Point out each Plasmodium parasite.
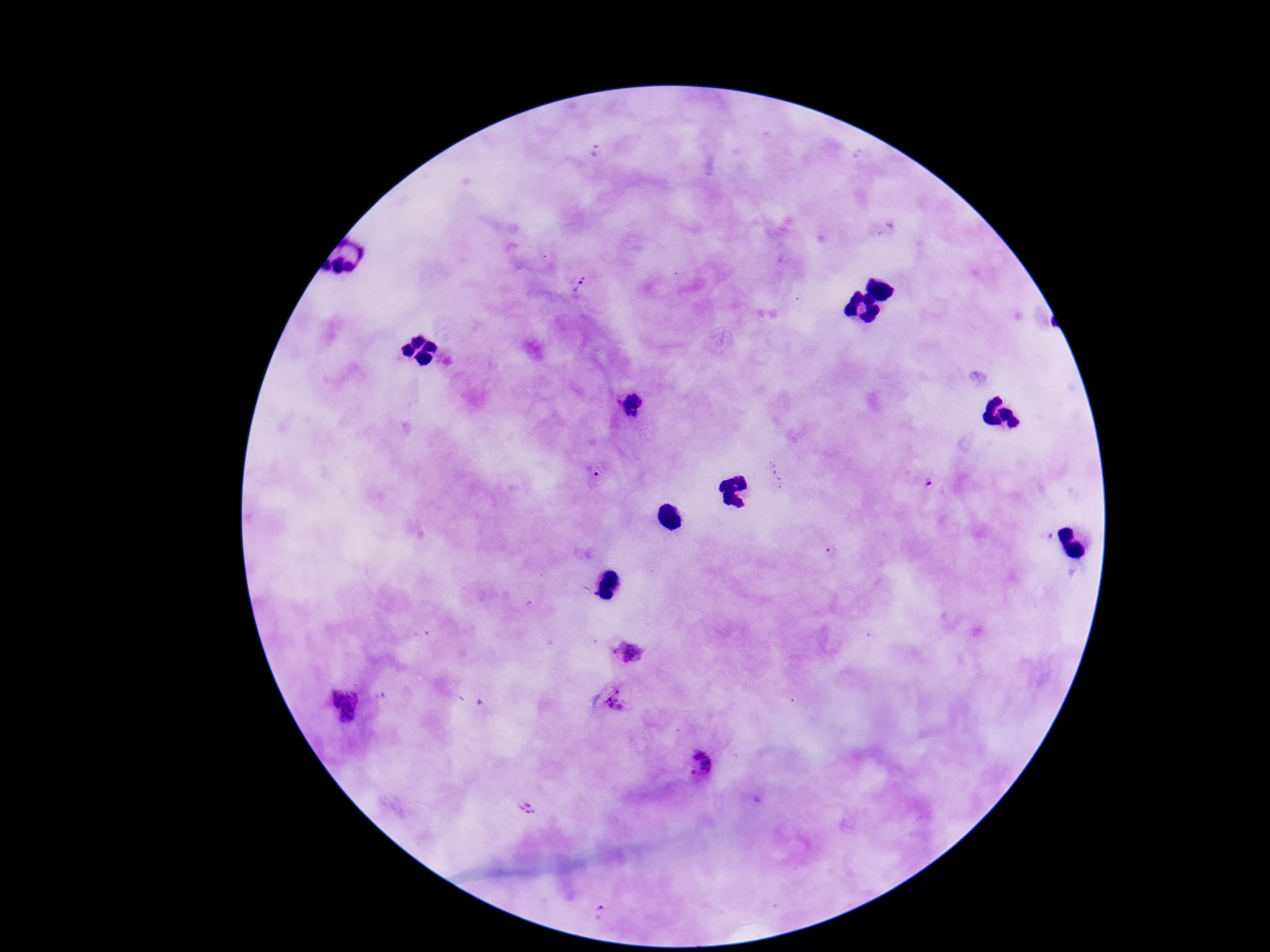
Approximate object centers, in pixels from the top-left corner.
Plasmodium parasites: (x=595, y=152), (x=580, y=283), (x=632, y=402), (x=596, y=474), (x=929, y=486), (x=1045, y=536), (x=831, y=550), (x=629, y=653), (x=379, y=696), (x=615, y=703), (x=344, y=705), (x=702, y=766), (x=532, y=809), (x=601, y=916).

patient malaria status = infected
preparation = thick blood film
magnification = 100x
field of view = single
image size = 1270×952 pixels
capture = smartphone camera through the microscope eyepiece
stain = Giemsa